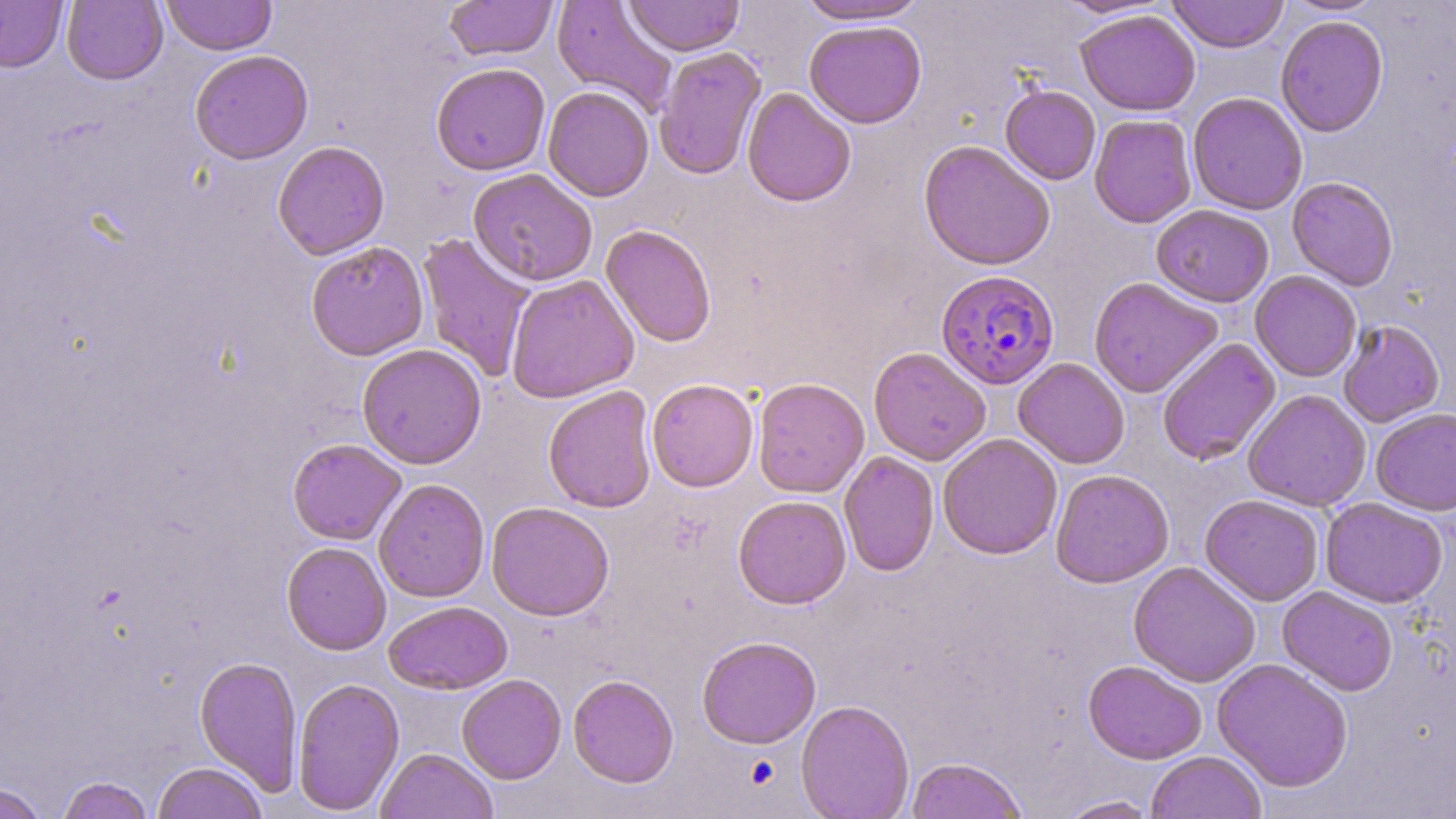
slide-level diagnosis = Plasmodium falciparum
stain = May-Grünwald-Giemsa
image size = 1456×819 pixels
field of view = single
Plasmodium falciparum-infected red blood cell locations = approximate bounding boxes as (x1,y1)-(x2,y2) corner pairs in pixels: (935,269)-(1059,390)
uninfected red blood cell locations = approximate bounding boxes as (x1,y1)-(x2,y2) corner pairs in pixels: (0,0)-(67,72), (62,0)-(168,85), (161,0)-(276,55), (445,0)-(557,62), (552,0)-(678,117), (624,0)-(745,57), (795,0)-(929,24), (1055,0)-(1172,19), (1166,0)-(1289,53), (1280,0)-(1388,15), (65,1)-(277,68), (1075,9)-(1200,116), (1275,15)-(1389,137), (804,21)-(927,129), (653,46)-(766,180), (189,49)-(313,165), (431,62)-(551,175), (1000,85)-(1101,184), (543,86)-(655,201), (742,87)-(856,207), (1187,92)-(1308,215), (1089,114)-(1197,228), (272,140)-(390,259), (918,140)-(1056,270), (467,167)-(597,287), (1287,177)-(1399,291), (1151,205)-(1274,307), (600,223)-(717,348), (416,232)-(536,383), (306,240)-(429,361), (1250,271)-(1361,381), (505,274)-(639,403), (1088,277)-(1223,398), (1337,319)-(1445,427), (1157,338)-(1281,466), (356,343)-(487,469), (868,346)-(991,466), (1013,358)-(1130,469), (752,377)-(869,497), (647,378)-(759,492), (542,385)-(658,513), (1242,389)-(1371,511), (1371,407)-(1456,516), (937,433)-(1063,560), (287,438)-(407,545), (839,451)-(939,577), (1050,468)-(1175,588), (373,478)-(490,603), (1200,494)-(1324,606), (733,495)-(852,609), (1320,498)-(1448,608), (486,501)-(615,621), (281,541)-(391,655), (1128,561)-(1261,687), (1277,586)-(1398,696), (383,600)-(513,695), (697,636)-(821,748), (194,655)-(303,794), (1212,658)-(1354,792), (1083,660)-(1207,764), (457,674)-(567,784), (568,674)-(679,787), (292,676)-(405,815), (795,699)-(914,819), (375,748)-(498,819), (1145,751)-(1267,818), (905,757)-(1028,819), (152,761)-(268,819), (56,776)-(155,819), (0,782)-(48,819), (1055,796)-(1162,818)
preparation = thin blood smear
modality = optical microscopy
magnification = 1000x